Assess the morphology of the red blood cells.
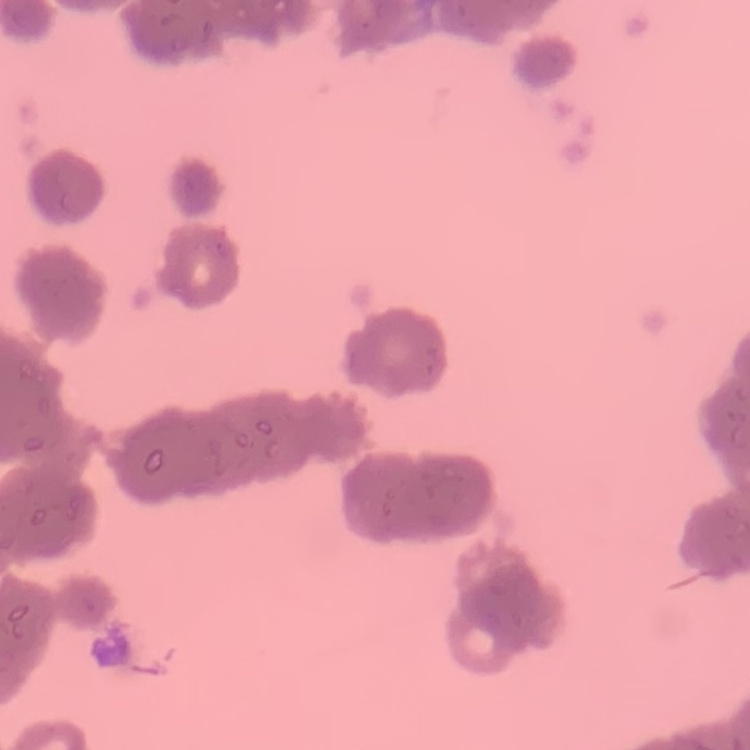

Rouleaux formation.

{
  "preparation": "thin blood smear",
  "image_type": "one tile cut from a larger photomicrograph",
  "stain": "Field's or Giemsa"
}